State which parasite is depicted.
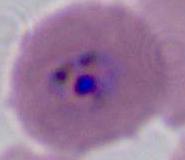
Plasmodium.

magnification = 400x or 1000x
modality = micrograph